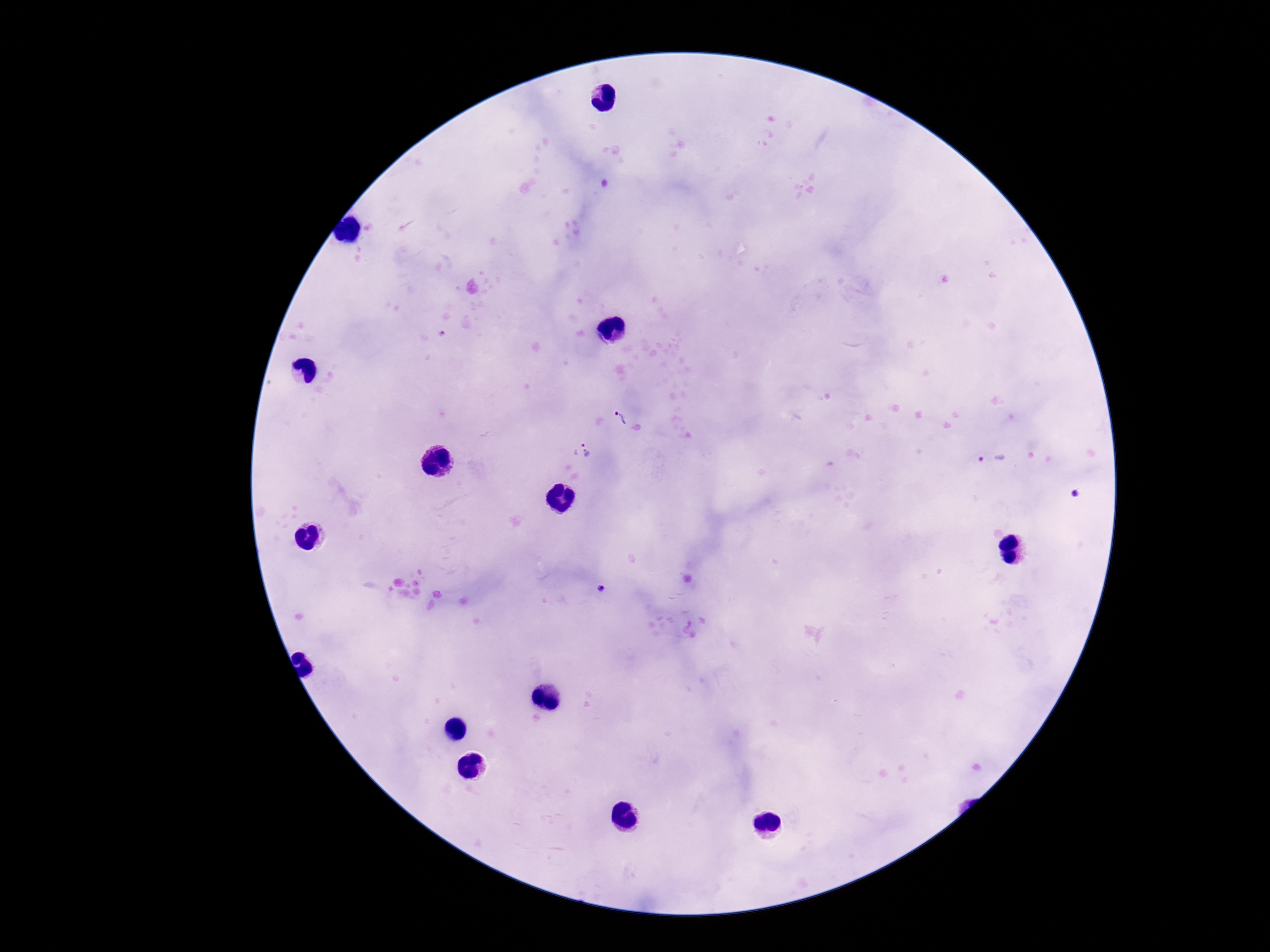 Approximate object centers, in pixels from the top-left corner. Plasmodium parasite locations: (x=620, y=417), (x=588, y=450), (x=993, y=459), (x=1076, y=494), (x=602, y=590). One field from this slide. 100x magnification. Smartphone photograph taken through the microscope eyepiece. Image is 1270×952 pixels. Patient malaria status: positive. Thick blood smear. Giemsa-stained preparation.